Identify the parasite.
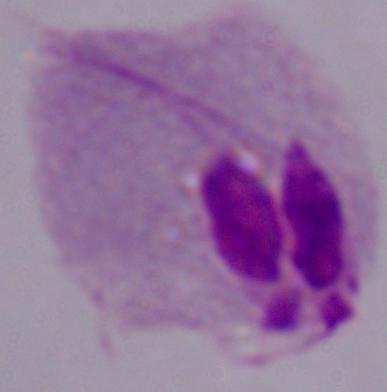

This is a trichomonad.

1000x magnification. Micrograph.